Assess this cell for malaria.
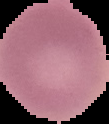
It is uninfected.

preparation = thin blood smear
image type = segmented cell region on a black background
image size = 109×124 pixels